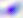

Summary:
  - Modality: micrograph
  - Identification: Toxoplasma gondii
  - Magnification: 400x